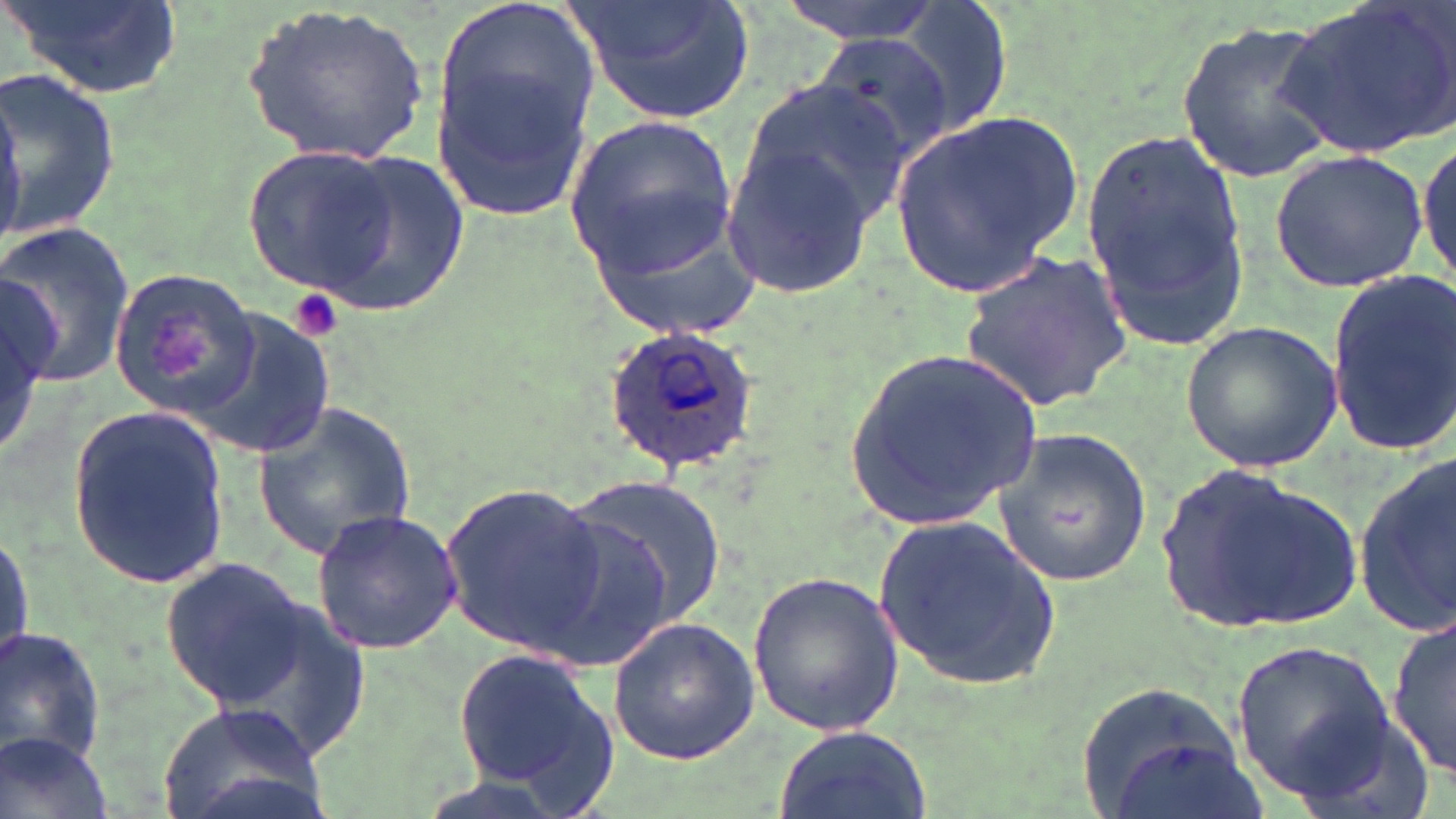

Approximate bounding boxes as named x1/y1/x2/y2 corners in pixels. Platelet locations: (x1=285, y1=288, x2=346, y2=342). Plasmodium ovale-infected red blood cell locations: (x1=602, y1=327, x2=759, y2=477). Uninfected red blood cell locations: (x1=433, y1=0, x2=599, y2=159), (x1=566, y1=0, x2=761, y2=124), (x1=771, y1=0, x2=947, y2=40), (x1=891, y1=0, x2=1017, y2=138), (x1=1276, y1=0, x2=1456, y2=157), (x1=9, y1=1, x2=181, y2=99), (x1=244, y1=3, x2=433, y2=166), (x1=1174, y1=19, x2=1338, y2=187), (x1=811, y1=31, x2=953, y2=170), (x1=428, y1=60, x2=595, y2=221), (x1=1, y1=62, x2=124, y2=247), (x1=730, y1=82, x2=908, y2=238), (x1=0, y1=85, x2=24, y2=238), (x1=891, y1=109, x2=1082, y2=298), (x1=564, y1=118, x2=740, y2=276), (x1=1079, y1=127, x2=1248, y2=350), (x1=1416, y1=133, x2=1454, y2=292), (x1=723, y1=137, x2=889, y2=300), (x1=242, y1=144, x2=400, y2=298), (x1=1270, y1=149, x2=1431, y2=293), (x1=303, y1=150, x2=467, y2=317), (x1=586, y1=204, x2=766, y2=342), (x1=0, y1=224, x2=137, y2=388), (x1=959, y1=249, x2=1135, y2=413), (x1=110, y1=265, x2=265, y2=416), (x1=1322, y1=269, x2=1456, y2=454), (x1=0, y1=274, x2=54, y2=456), (x1=188, y1=307, x2=334, y2=460), (x1=1182, y1=322, x2=1344, y2=475), (x1=841, y1=346, x2=1046, y2=534), (x1=253, y1=398, x2=419, y2=560), (x1=69, y1=404, x2=230, y2=589), (x1=995, y1=428, x2=1153, y2=587), (x1=1353, y1=457, x2=1456, y2=636), (x1=1156, y1=464, x2=1364, y2=632), (x1=563, y1=477, x2=726, y2=630), (x1=440, y1=478, x2=604, y2=655), (x1=524, y1=505, x2=675, y2=674), (x1=869, y1=507, x2=1061, y2=695), (x1=307, y1=509, x2=463, y2=656), (x1=0, y1=522, x2=33, y2=680), (x1=160, y1=557, x2=311, y2=708), (x1=745, y1=572, x2=907, y2=737), (x1=189, y1=578, x2=379, y2=766), (x1=607, y1=614, x2=763, y2=765), (x1=1390, y1=615, x2=1454, y2=779), (x1=0, y1=629, x2=106, y2=768), (x1=1230, y1=640, x2=1395, y2=798), (x1=450, y1=643, x2=625, y2=813), (x1=1082, y1=682, x2=1254, y2=819), (x1=153, y1=701, x2=331, y2=819), (x1=772, y1=723, x2=933, y2=819), (x1=0, y1=731, x2=116, y2=819). Slide-level diagnosis: Plasmodium ovale. Image is 1456×819 pixels. May-Grünwald-Giemsa-stained preparation. Single field of view. Thin blood smear. Captured at 1000x magnification. Optical microscopy.